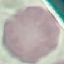
result = no malaria parasites seen
capture = smartphone through the microscope eyepiece
image type = automatically extracted cell patch, resized to 64 × 64 pixels
preparation = thin blood smear
stain = Giemsa